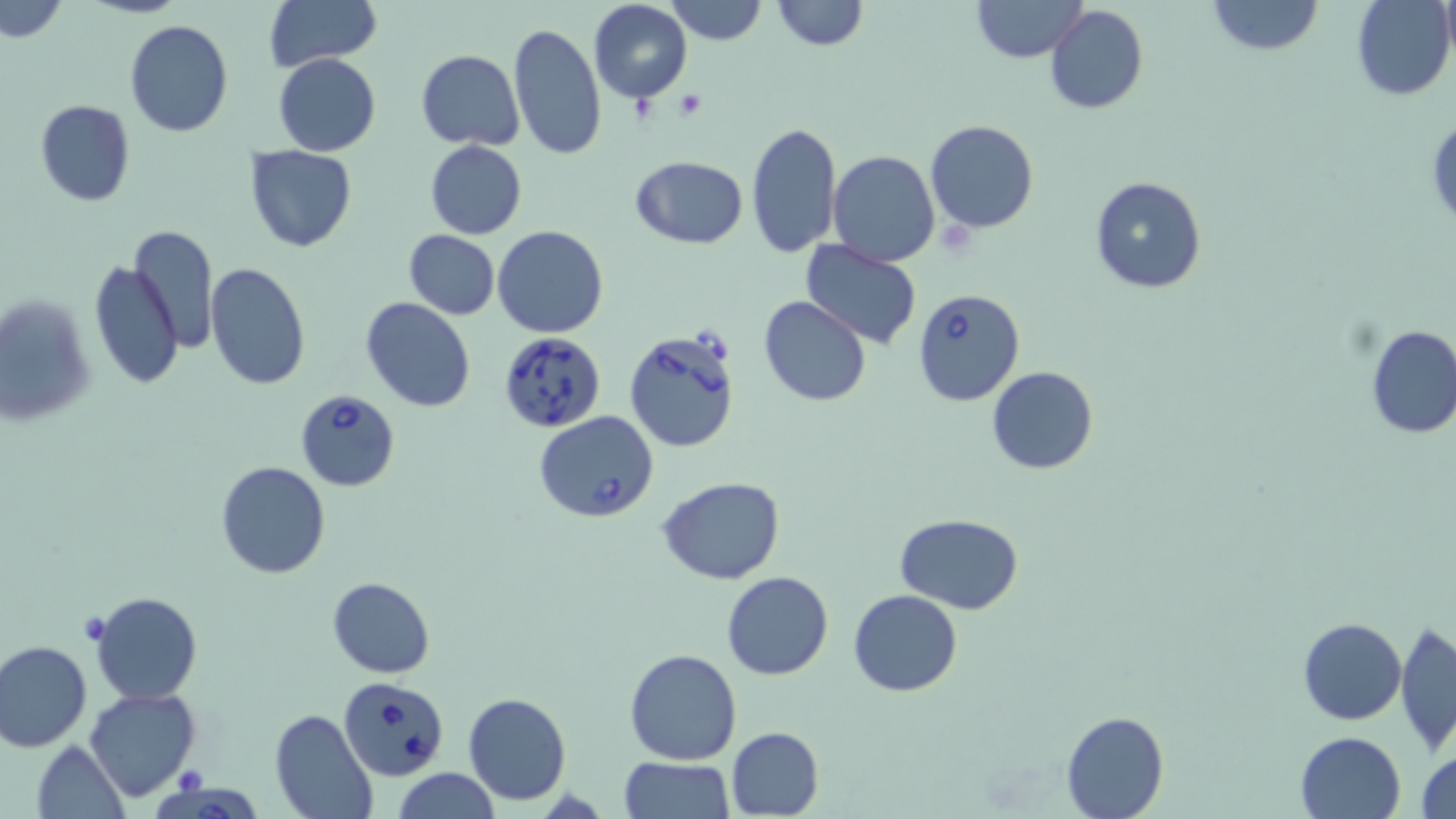 Approximate bounding boxes as [x1, y1, x2, y2] in pixels. Platelet locations: [674, 89, 707, 119], [628, 94, 658, 128], [82, 615, 107, 641], [173, 766, 203, 794]. Uninfected red blood cell locations: [2, 0, 68, 42], [261, 0, 382, 71], [587, 0, 694, 103], [770, 0, 868, 49], [971, 0, 1087, 64], [1207, 0, 1323, 56], [1349, 0, 1455, 100], [1438, 0, 1455, 65], [663, 1, 768, 46], [1045, 5, 1148, 114], [125, 19, 233, 137], [508, 21, 605, 160], [416, 49, 524, 149], [274, 53, 380, 156], [258, 54, 369, 248], [34, 101, 135, 205], [1426, 112, 1456, 227], [746, 120, 841, 258], [924, 120, 1038, 234], [426, 139, 527, 238], [244, 144, 358, 252], [828, 149, 939, 265], [629, 156, 749, 249], [1088, 175, 1210, 294], [129, 224, 221, 354], [493, 225, 609, 339], [403, 231, 500, 319], [799, 238, 924, 350], [86, 259, 184, 391], [206, 262, 312, 392], [1, 294, 97, 428], [758, 296, 871, 406], [361, 297, 477, 414], [1363, 323, 1456, 440], [986, 365, 1099, 475], [216, 461, 331, 579], [658, 477, 786, 584], [894, 513, 1024, 611], [721, 571, 834, 679], [327, 577, 435, 677], [849, 590, 963, 696], [87, 591, 203, 705], [1297, 616, 1407, 724], [1394, 621, 1456, 755], [1, 640, 92, 753], [625, 649, 743, 765], [84, 687, 200, 801], [463, 692, 570, 805], [269, 711, 378, 819], [1061, 711, 1169, 819], [726, 726, 824, 818], [1296, 731, 1407, 819], [31, 740, 129, 819], [1415, 744, 1456, 819], [618, 756, 734, 819], [392, 768, 502, 819]. Babesia divergens-infected red blood cell locations: [914, 288, 1024, 406], [623, 328, 741, 451], [500, 332, 606, 433], [295, 388, 400, 491], [534, 412, 659, 523], [338, 677, 448, 779], [153, 782, 261, 819]. Slide-level diagnosis: Babesia divergens. Single field of view. May-Grünwald-Giemsa stain. Image is 1456×819 pixels. Thin blood film. Captured at 1000x magnification. Optical microscopy.